Name the parasite shown.
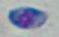
Toxoplasma gondii.

Summary:
  - Modality: micrograph
  - Magnification: 1000x